Outline each blood parasite and name the species.
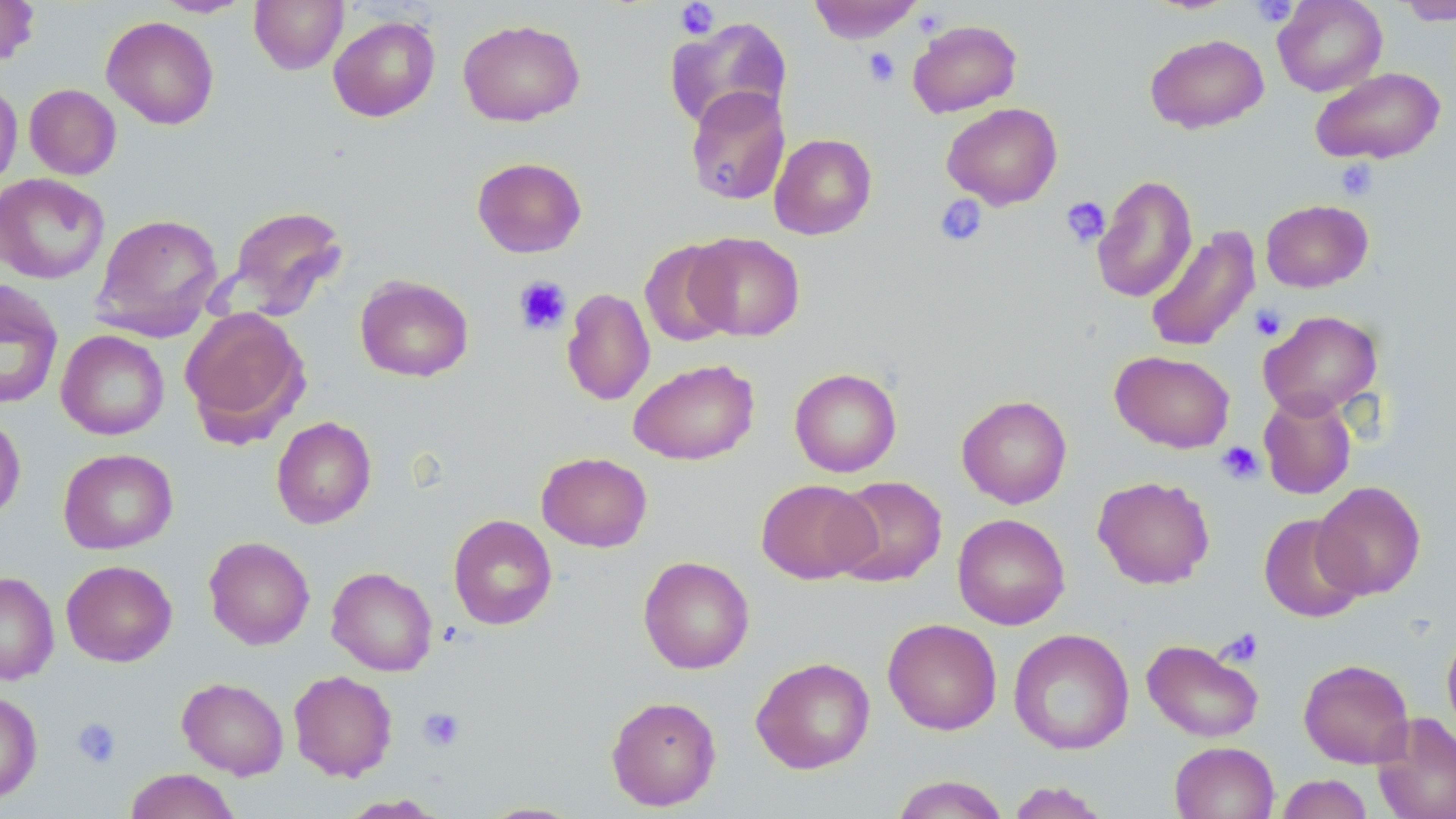
No blood parasites observed.

Approximate bounding boxes as named x1/y1/x2/y2 corners in pixels. Uninfected red blood cell locations: (x1=0, y1=0, x2=40, y2=67), (x1=249, y1=0, x2=348, y2=74), (x1=809, y1=0, x2=923, y2=43), (x1=1272, y1=0, x2=1387, y2=96), (x1=154, y1=1, x2=253, y2=17), (x1=1398, y1=1, x2=1456, y2=25), (x1=328, y1=15, x2=440, y2=122), (x1=101, y1=16, x2=219, y2=130), (x1=665, y1=16, x2=793, y2=131), (x1=458, y1=18, x2=586, y2=126), (x1=908, y1=19, x2=1022, y2=117), (x1=1145, y1=33, x2=1269, y2=134), (x1=1311, y1=66, x2=1446, y2=164), (x1=0, y1=80, x2=23, y2=192), (x1=24, y1=84, x2=121, y2=179), (x1=685, y1=86, x2=790, y2=206), (x1=941, y1=102, x2=1063, y2=209), (x1=769, y1=133, x2=877, y2=240), (x1=471, y1=156, x2=587, y2=258), (x1=0, y1=173, x2=110, y2=284), (x1=1091, y1=174, x2=1197, y2=303), (x1=1260, y1=199, x2=1374, y2=293), (x1=221, y1=204, x2=349, y2=322), (x1=91, y1=213, x2=224, y2=341), (x1=1143, y1=224, x2=1261, y2=353), (x1=686, y1=232, x2=805, y2=341), (x1=639, y1=240, x2=738, y2=347), (x1=355, y1=275, x2=474, y2=382), (x1=0, y1=280, x2=64, y2=410), (x1=562, y1=287, x2=655, y2=406), (x1=180, y1=307, x2=309, y2=444), (x1=1259, y1=310, x2=1382, y2=419), (x1=56, y1=330, x2=169, y2=440), (x1=1110, y1=350, x2=1235, y2=453), (x1=628, y1=359, x2=760, y2=465), (x1=789, y1=367, x2=902, y2=478), (x1=1258, y1=391, x2=1357, y2=500), (x1=956, y1=394, x2=1072, y2=508), (x1=0, y1=413, x2=26, y2=521), (x1=271, y1=415, x2=376, y2=529), (x1=58, y1=448, x2=178, y2=554), (x1=536, y1=452, x2=653, y2=552), (x1=1093, y1=475, x2=1215, y2=589), (x1=829, y1=476, x2=946, y2=587), (x1=756, y1=479, x2=878, y2=584), (x1=1312, y1=480, x2=1426, y2=600), (x1=1258, y1=513, x2=1365, y2=623), (x1=448, y1=514, x2=557, y2=630), (x1=953, y1=514, x2=1070, y2=630), (x1=204, y1=536, x2=315, y2=649), (x1=638, y1=555, x2=754, y2=674), (x1=61, y1=560, x2=177, y2=666), (x1=326, y1=567, x2=437, y2=676), (x1=0, y1=571, x2=59, y2=685), (x1=882, y1=618, x2=1002, y2=735), (x1=1442, y1=627, x2=1456, y2=740), (x1=1008, y1=628, x2=1134, y2=755), (x1=1142, y1=638, x2=1264, y2=742), (x1=751, y1=656, x2=875, y2=774), (x1=1298, y1=658, x2=1415, y2=768), (x1=289, y1=670, x2=398, y2=781), (x1=177, y1=677, x2=289, y2=779), (x1=0, y1=690, x2=42, y2=803), (x1=606, y1=695, x2=722, y2=811), (x1=1372, y1=711, x2=1456, y2=819), (x1=1169, y1=741, x2=1279, y2=818), (x1=124, y1=768, x2=241, y2=819), (x1=1276, y1=774, x2=1374, y2=819), (x1=890, y1=775, x2=1011, y2=819), (x1=1005, y1=781, x2=1111, y2=818), (x1=338, y1=794, x2=446, y2=818), (x1=477, y1=801, x2=586, y2=818). Platelet locations: (x1=1250, y1=0, x2=1297, y2=27), (x1=675, y1=1, x2=720, y2=39), (x1=864, y1=48, x2=900, y2=86), (x1=1335, y1=158, x2=1378, y2=201), (x1=935, y1=195, x2=987, y2=247), (x1=1061, y1=196, x2=1109, y2=247), (x1=513, y1=275, x2=572, y2=335), (x1=1250, y1=304, x2=1287, y2=341), (x1=1216, y1=441, x2=1264, y2=485), (x1=1218, y1=627, x2=1264, y2=667), (x1=418, y1=706, x2=464, y2=751), (x1=71, y1=717, x2=122, y2=768). Slide-level diagnosis: no evidence of blood parasites. Thin blood film. 1000x magnification. May-Grünwald-Giemsa stain. Light microscopy. One field of a larger specimen. Image is 1456×819 pixels.